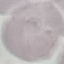
{
  "malaria_status": "uninfected",
  "capture": "smartphone camera at the microscope eyepiece",
  "preparation": "thin blood smear",
  "stain": "Giemsa",
  "image_type": "automatically extracted cell patch, resized to 64 × 64 pixels"
}